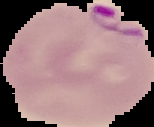
image type = segmented cell region with the area outside set to black
image size = 154×127 pixels
preparation = thin blood film
malaria status = parasitized